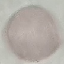
malaria status = uninfected
preparation = thin smear
image type = cell patch, automatically extracted from a larger field of view and resized to 64 × 64 pixels
capture = smartphone through the microscope eyepiece
stain = Giemsa